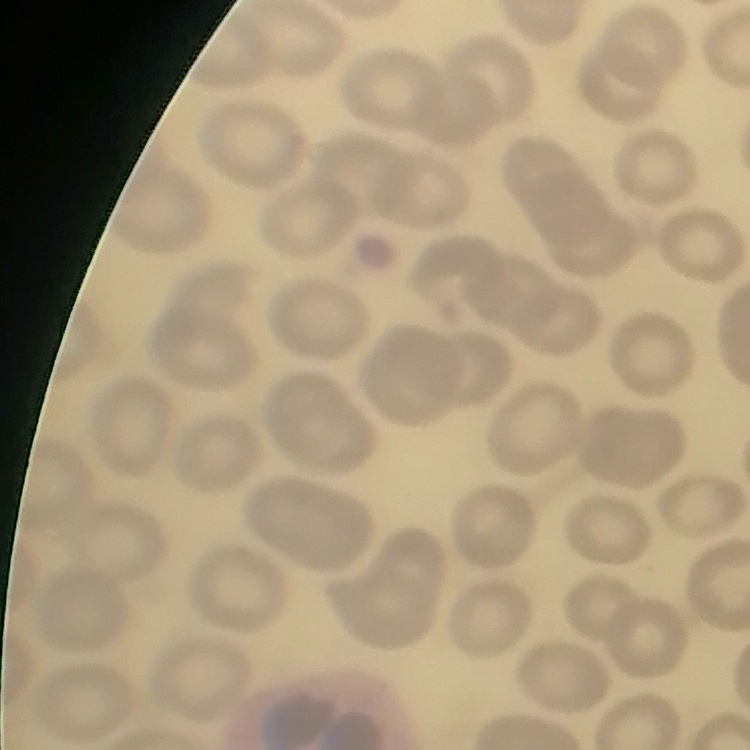

{
  "red_blood_cell_morphology": "no rouleaux formation",
  "stain": "Field's or Giemsa",
  "image_type": "square crop of a larger photomicrograph",
  "preparation": "thin peripheral smear"
}